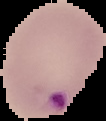

{
  "preparation": "thin blood film",
  "image_type": "segmented cell region with the area outside set to black",
  "result": "Plasmodium parasites identified",
  "image_size": "106×121 pixels"
}